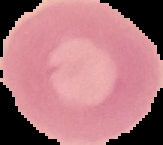

result: no Plasmodium parasites seen
image_size: 163×145 pixels
image_type: segmented cell region on a black background
preparation: thin blood smear